Outline each Plasmodium falciparum-infected red blood cell.
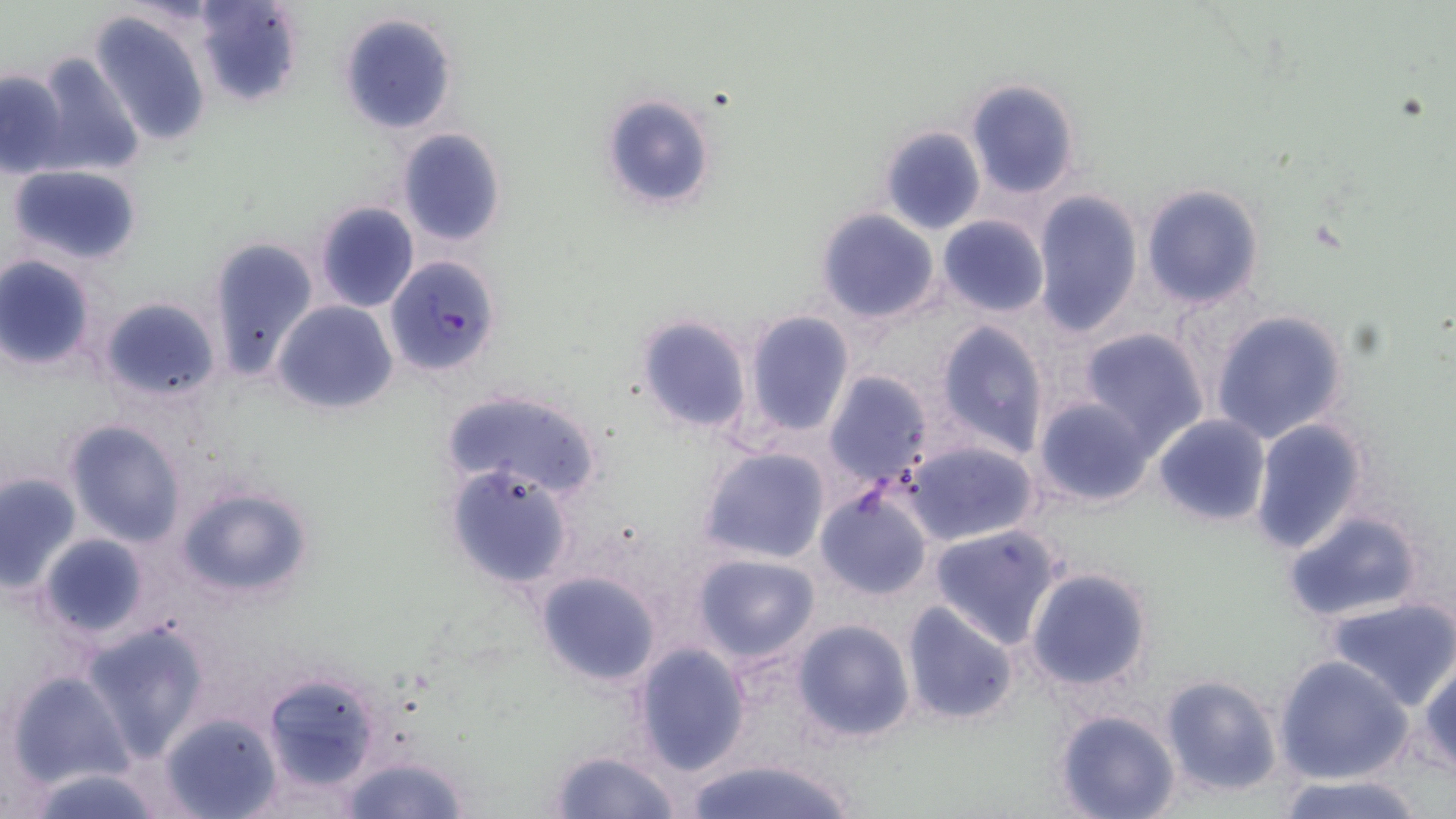

Approximate bounding boxes as (x1, y1, x2, y2) in pixels.
Plasmodium falciparum-infected red blood cells: (383, 255, 501, 377).

Uninfected red blood cell locations: (190, 0, 305, 109), (87, 10, 214, 149), (338, 12, 459, 134), (30, 50, 146, 181), (0, 69, 71, 179), (965, 78, 1081, 199), (602, 94, 718, 213), (880, 125, 985, 235), (395, 129, 506, 247), (6, 165, 144, 266), (1138, 182, 1266, 310), (1030, 189, 1144, 338), (314, 201, 420, 314), (814, 207, 941, 324), (938, 215, 1050, 317), (205, 236, 319, 381), (0, 254, 98, 370), (97, 296, 221, 403), (273, 301, 397, 416), (741, 309, 854, 438), (1209, 309, 1351, 445), (634, 312, 753, 436), (933, 322, 1048, 460), (1078, 326, 1210, 453), (823, 369, 933, 485), (439, 389, 604, 504), (1034, 397, 1156, 508), (1153, 413, 1271, 526), (1249, 417, 1370, 555), (64, 419, 186, 546), (902, 439, 1039, 545), (697, 446, 831, 566), (443, 464, 574, 591), (1, 471, 80, 593), (173, 484, 315, 601), (816, 488, 933, 601), (1283, 510, 1427, 625), (928, 523, 1066, 648), (38, 532, 151, 640), (690, 552, 820, 663), (1024, 566, 1156, 693), (534, 569, 664, 688), (1323, 594, 1456, 711), (900, 600, 1018, 725), (791, 619, 916, 745), (82, 620, 210, 760), (629, 642, 751, 776), (1274, 656, 1412, 785), (1417, 659, 1456, 777), (6, 669, 135, 791), (260, 669, 386, 792), (1158, 674, 1284, 798), (1053, 709, 1182, 819), (160, 712, 282, 819), (546, 749, 682, 819), (337, 751, 474, 818), (679, 756, 864, 819), (22, 767, 169, 819), (1272, 772, 1431, 819). Slide-level diagnosis: Plasmodium falciparum. Thin blood smear. Single field of view. May-Grünwald-Giemsa-stained preparation. Light microscopy. Captured at 1000x magnification. Image is 1456×819 pixels.